Assess this cell for malaria.
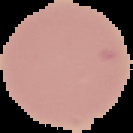
It is uninfected.

image size = 133×133 pixels
image type = segmented cell region on a black background
preparation = thin blood film